Describe the morphology of the erythrocytes.
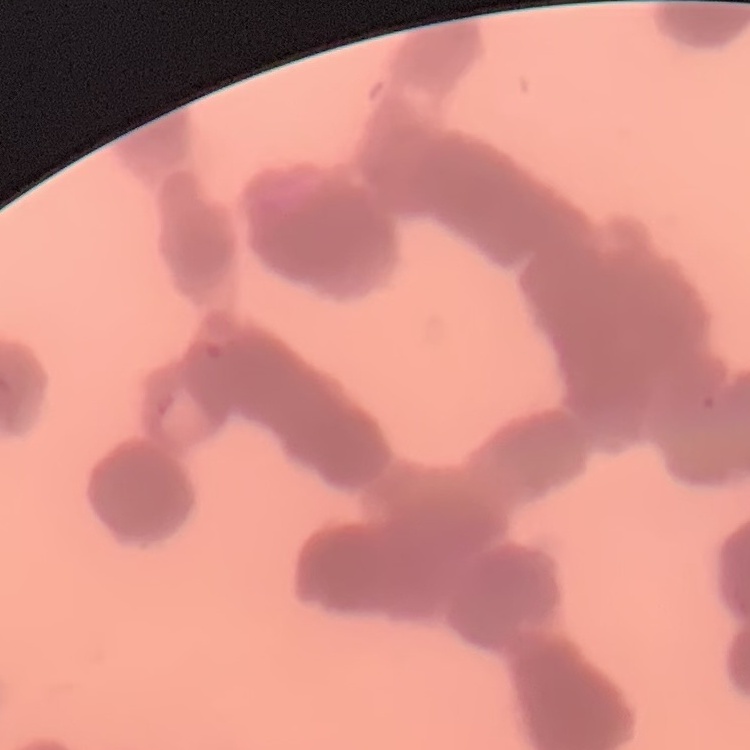

They show rouleaux formation.

Summary:
  - Stain: Field's or Giemsa
  - Preparation: thin blood smear
  - Image type: one tile cut from a larger photomicrograph